Describe the morphology of the red blood cells.
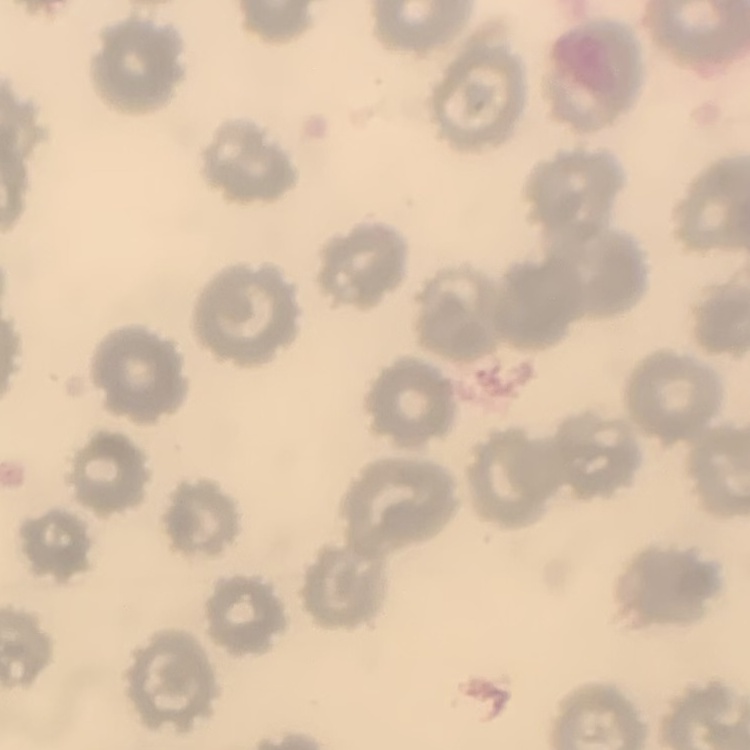

No rouleaux formation.

stain = Field's or Giemsa
image type = one tile cut from a larger photomicrograph
preparation = thin peripheral smear